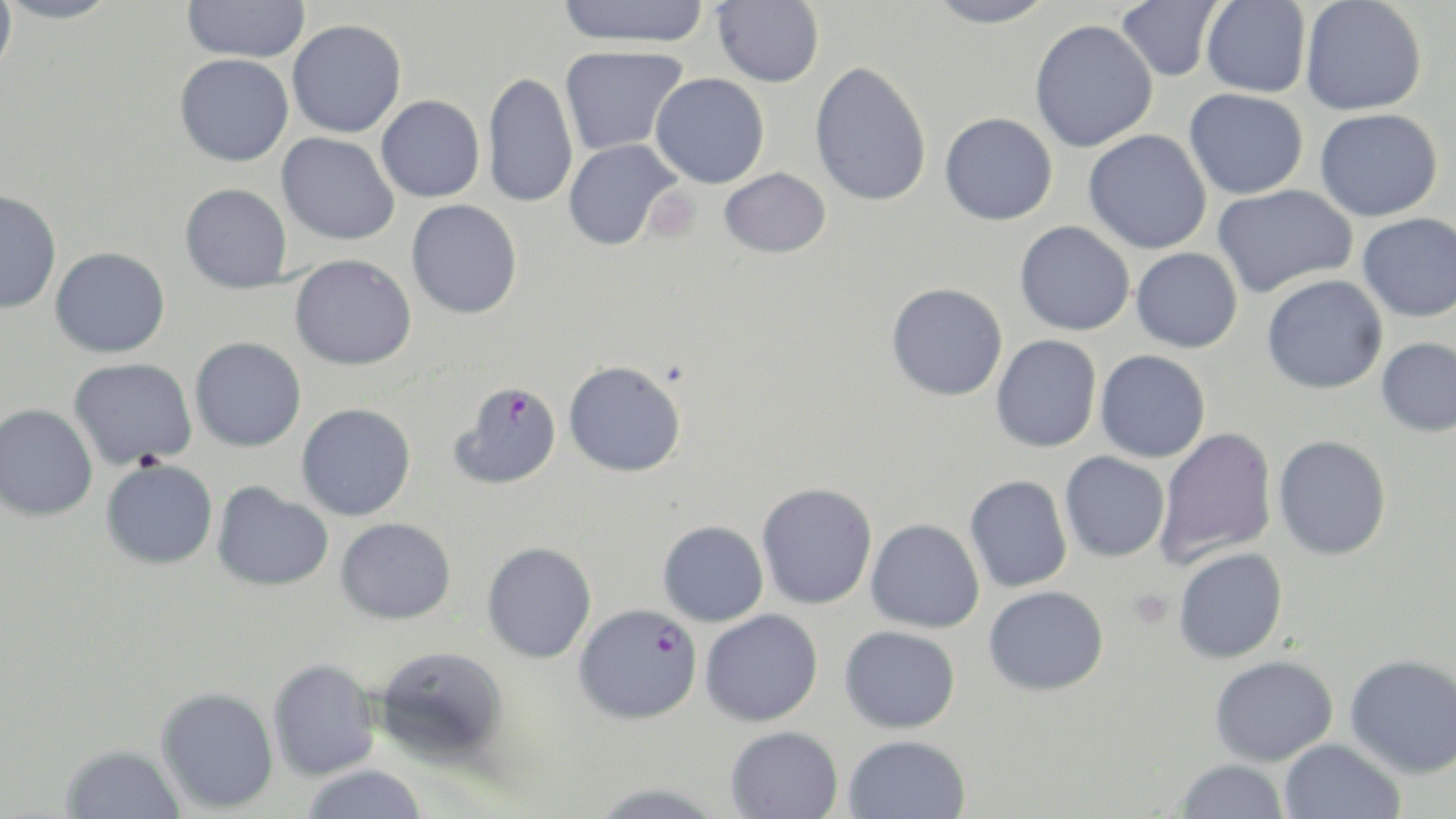

{
  "slide_level_diagnosis": "Plasmodium falciparum",
  "image_size": "1456×819 pixels",
  "field_of_view": "one of a larger specimen",
  "preparation": "thin blood smear",
  "plasmodium_falciparum_infected_red_blood_cell_locations": "approximate bounding boxes as [x1, y1, x2, y2] in pixels: [449, 381, 562, 491], [574, 603, 702, 724]",
  "uninfected_red_blood_cell_locations": "approximate bounding boxes as [x1, y1, x2, y2] in pixels: [0, 0, 17, 80], [0, 0, 121, 24], [182, 0, 310, 63], [557, 0, 709, 48], [712, 0, 824, 88], [924, 0, 1056, 28], [1116, 0, 1222, 82], [1300, 0, 1427, 116], [1201, 1, 1312, 98], [287, 19, 406, 138], [1029, 19, 1158, 153], [559, 45, 688, 156], [174, 53, 294, 166], [809, 60, 932, 207], [482, 71, 578, 209], [650, 73, 770, 188], [1184, 88, 1308, 199], [376, 95, 485, 202], [1315, 108, 1443, 222], [940, 112, 1057, 225], [1083, 130, 1212, 254], [277, 132, 399, 245], [563, 139, 682, 251], [719, 167, 831, 258], [180, 183, 292, 294], [1212, 184, 1357, 298], [0, 190, 61, 314], [406, 200, 522, 319], [1358, 213, 1456, 322], [1015, 220, 1134, 336], [50, 247, 170, 358], [1131, 247, 1243, 353], [289, 254, 416, 370], [1261, 275, 1387, 394], [886, 282, 1008, 401], [990, 335, 1101, 453], [189, 337, 307, 452], [1376, 337, 1456, 437], [1095, 350, 1211, 463], [68, 357, 198, 470], [564, 360, 687, 478], [0, 403, 98, 522], [296, 403, 416, 521], [1155, 427, 1277, 567], [1273, 435, 1392, 561], [1059, 451, 1170, 562], [100, 458, 218, 569], [964, 474, 1073, 593], [212, 482, 333, 592], [756, 482, 877, 609], [336, 517, 456, 624], [866, 518, 984, 633], [657, 521, 768, 626], [482, 542, 596, 664], [1173, 547, 1288, 664], [983, 585, 1108, 696], [699, 609, 823, 727], [839, 625, 960, 733], [374, 645, 509, 765], [1345, 654, 1456, 778], [1209, 655, 1338, 766], [267, 658, 380, 781], [155, 687, 279, 814], [725, 725, 844, 818], [842, 734, 971, 819], [1278, 738, 1406, 819], [60, 745, 186, 819], [1174, 759, 1290, 819], [301, 765, 427, 819], [587, 783, 727, 819]",
  "platelet_locations": "approximate bounding boxes as [x1, y1, x2, y2] in pixels: [645, 189, 700, 243]",
  "magnification": "1000x",
  "stain": "May-Grünwald-Giemsa",
  "modality": "light microscopy"
}